State which parasite is depicted.
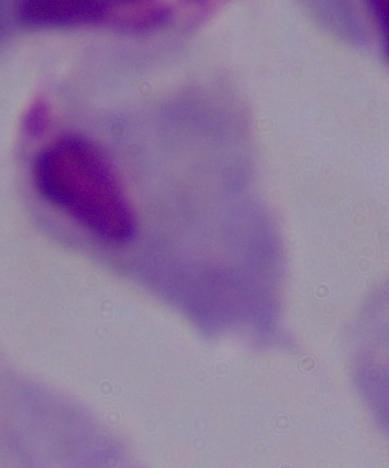
This is a trichomonad.

Summary:
  - Modality: micrograph
  - Magnification: 1000x